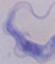
Summary:
  - Magnification: 1000x
  - Identification: trypanosome
  - Modality: micrograph